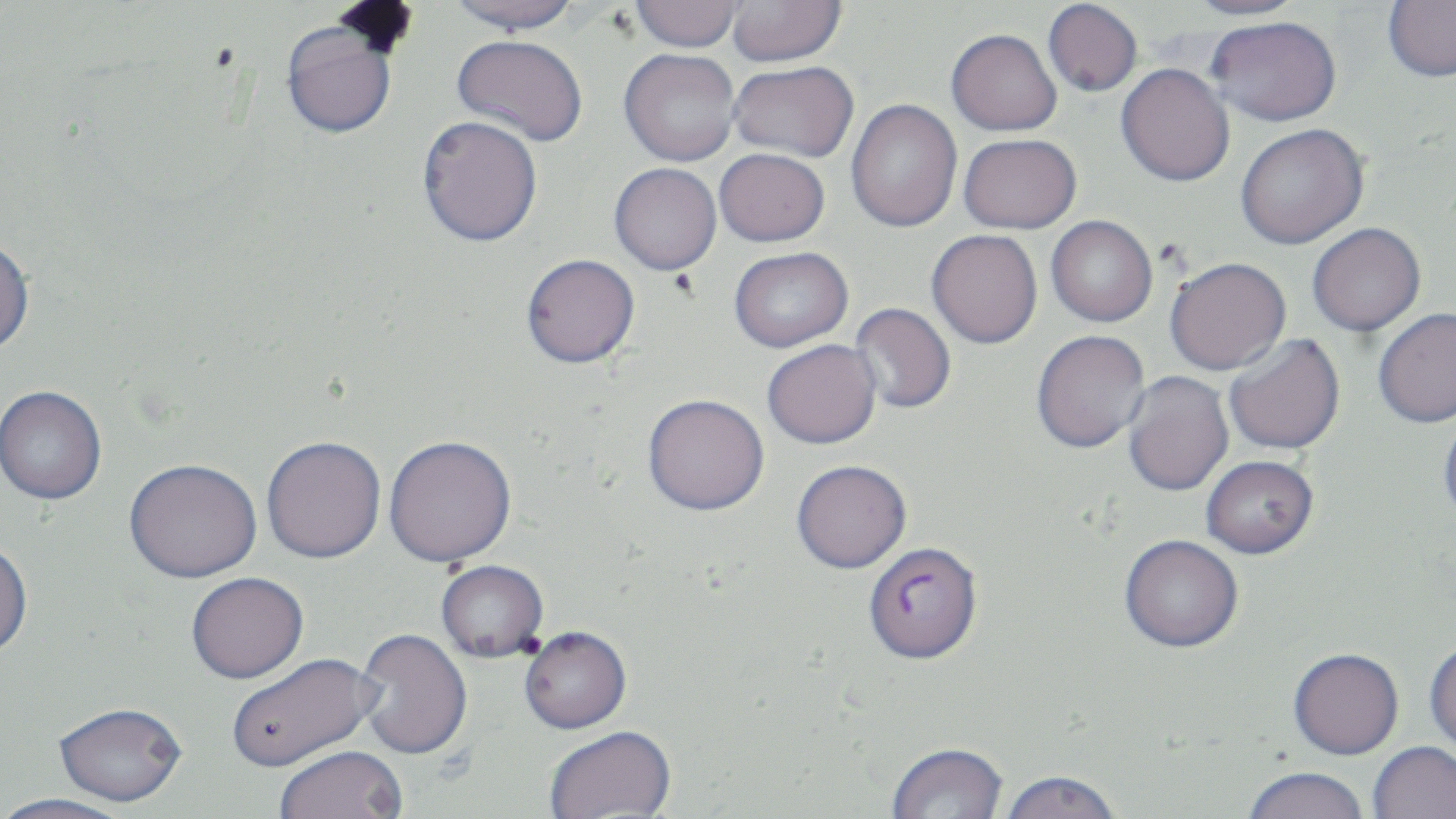
slide_level_diagnosis: Plasmodium falciparum
uninfected_red_blood_cell_locations: 'approximate bounding boxes as (x1,y1)-(x2,y2) corner pairs in pixels: (446,0)-(582,34), (631,0)-(743,52), (726,0)-(846,67), (1043,0)-(1142,96), (1183,0)-(1311,20), (1383,0)-(1456,81), (1207,16)-(1341,126), (280,20)-(399,139), (947,28)-(1062,136), (452,34)-(588,146), (619,48)-(741,166), (729,61)-(859,162), (1116,63)-(1235,186), (845,98)-(962,233), (417,115)-(543,247), (1235,124)-(1369,249), (958,133)-(1081,234), (714,148)-(830,247), (609,162)-(722,275), (1046,215)-(1158,327), (1307,222)-(1426,337), (926,229)-(1043,349), (0,237)-(35,356), (729,247)-(853,352), (521,253)-(640,368), (1165,257)-(1291,376), (850,302)-(957,414), (1373,307)-(1456,428), (1031,329)-(1150,453), (1223,334)-(1346,456), (762,339)-(882,449), (1122,372)-(1234,497), (0,386)-(107,505), (642,394)-(769,516), (1438,411)-(1456,528), (383,435)-(517,567), (261,436)-(387,565), (1201,455)-(1319,558), (123,459)-(262,584), (791,460)-(912,574), (1119,534)-(1244,652), (0,541)-(33,660), (435,560)-(549,664), (186,573)-(309,685), (519,627)-(632,736), (354,629)-(473,761), (1424,642)-(1456,761), (1288,647)-(1404,759), (226,653)-(380,774), (53,704)-(187,809), (544,728)-(677,818), (1368,741)-(1456,819), (886,743)-(1008,819), (275,747)-(407,819), (1242,766)-(1370,819), (998,772)-(1123,819), (0,794)-(134,819)'
plasmodium_falciparum_infected_red_blood_cell_locations: 'approximate bounding boxes as (x1,y1)-(x2,y2) corner pairs in pixels: (863,541)-(983,665)'
image_size: 1456×819 pixels
preparation: thin blood smear
stain: May-Grünwald-Giemsa
magnification: 1000x
field_of_view: single
modality: light microscopy